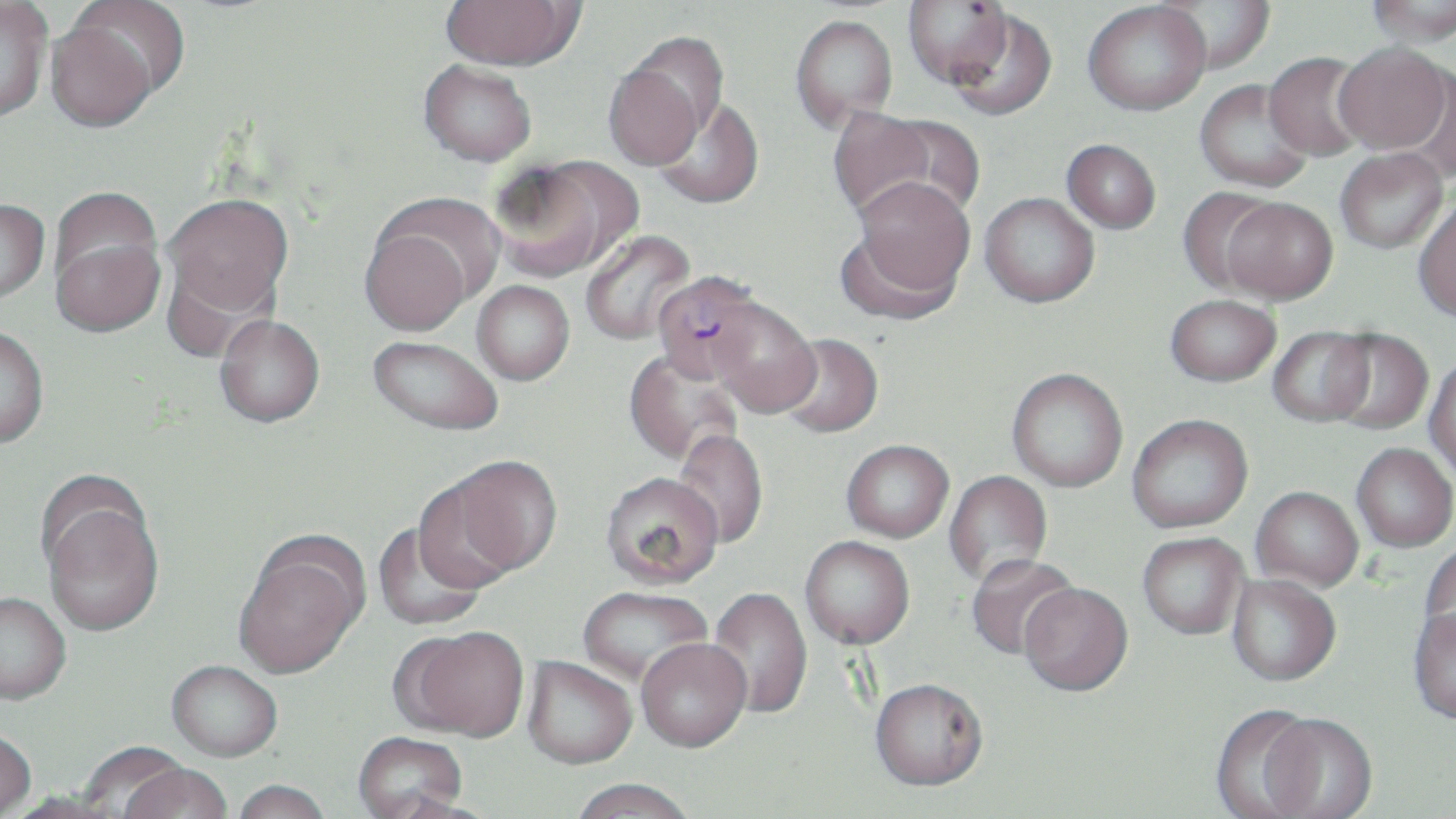

Summary:
  - Coordinate format: approximate bounding boxes as (x1, y1, x2, y2) in pixels
  - Uninfected red blood cell locations: (0, 0, 51, 122), (67, 0, 191, 99), (440, 0, 581, 70), (903, 0, 1013, 89), (1364, 0, 1455, 46), (1082, 1, 1211, 115), (1151, 1, 1275, 76), (948, 9, 1058, 120), (789, 15, 897, 132), (46, 21, 159, 132), (621, 31, 729, 143), (1334, 42, 1452, 154), (1263, 52, 1372, 161), (418, 59, 537, 166), (602, 62, 707, 169), (1403, 64, 1456, 184), (1195, 80, 1315, 193), (653, 96, 764, 209), (825, 107, 944, 221), (870, 114, 984, 222), (1061, 139, 1161, 233), (1335, 147, 1449, 254), (489, 156, 633, 282), (848, 176, 976, 309), (1177, 187, 1284, 297), (980, 192, 1100, 307), (162, 193, 294, 318), (1221, 197, 1338, 304), (0, 198, 49, 304), (1413, 198, 1456, 322), (360, 225, 471, 336), (580, 228, 696, 346), (50, 231, 164, 337), (162, 256, 277, 364), (472, 280, 575, 385), (1165, 294, 1281, 387), (708, 299, 820, 418), (215, 314, 325, 427), (1, 325, 49, 449), (1268, 327, 1375, 427), (1324, 329, 1434, 435), (776, 334, 883, 438), (368, 335, 504, 435), (623, 349, 744, 468), (1424, 355, 1456, 485), (1006, 367, 1129, 492), (1127, 413, 1253, 532), (670, 429, 769, 549), (841, 439, 954, 542), (1352, 443, 1455, 552), (443, 454, 564, 579), (943, 470, 1053, 589), (600, 471, 724, 589), (412, 476, 521, 594), (1251, 486, 1364, 591), (41, 493, 165, 636), (372, 522, 488, 631), (1137, 532, 1249, 639), (800, 535, 915, 649), (233, 536, 368, 680), (1420, 541, 1456, 653), (965, 554, 1081, 661), (1227, 574, 1341, 686), (1019, 583, 1133, 697), (577, 585, 712, 687), (706, 586, 813, 720), (0, 592, 71, 706), (1409, 607, 1456, 725), (401, 627, 530, 742), (636, 637, 752, 753), (521, 657, 637, 771), (166, 661, 282, 763), (870, 681, 989, 794), (1210, 705, 1323, 819), (1259, 715, 1378, 819), (0, 730, 36, 819), (352, 733, 469, 819), (78, 743, 192, 817), (121, 765, 233, 819), (230, 781, 333, 819), (568, 781, 699, 819), (3, 792, 125, 818)
  - Plasmodium falciparum-infected red blood cell locations: (652, 271, 766, 382)
  - Slide-level diagnosis: Plasmodium falciparum
  - Magnification: 1000x
  - Field of view: single
  - Image size: 1456×819 pixels
  - Stain: May-Grünwald-Giemsa
  - Modality: light microscopy
  - Preparation: thin blood film